Assess the morphology of the erythrocytes.
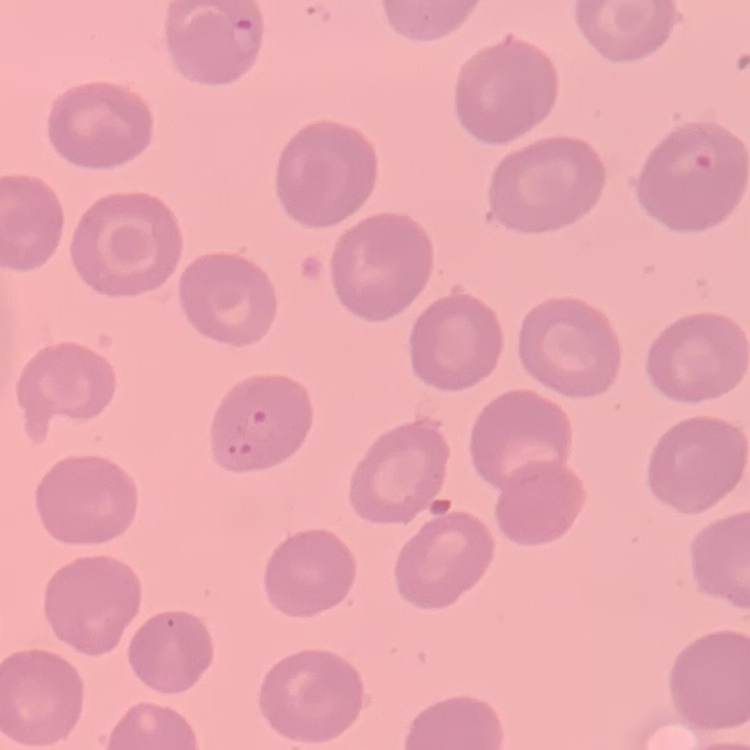
They show no rouleaux formation.

Thin blood smear. Square crop of a larger photomicrograph. Field's or Giemsa stain.